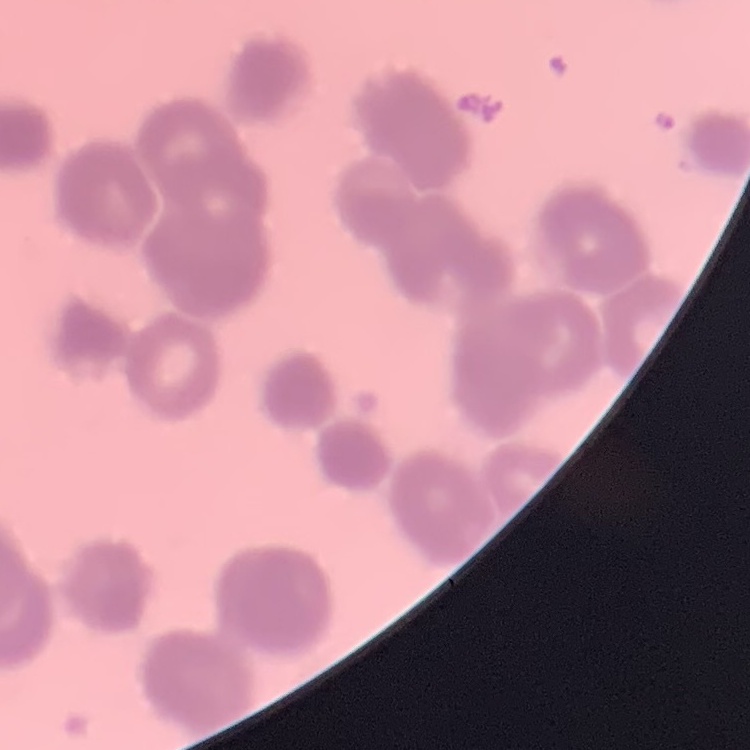
The erythrocytes exhibit rouleaux formation. Stained with either Field's or Giemsa. Thin peripheral smear. Square crop of a larger photomicrograph.